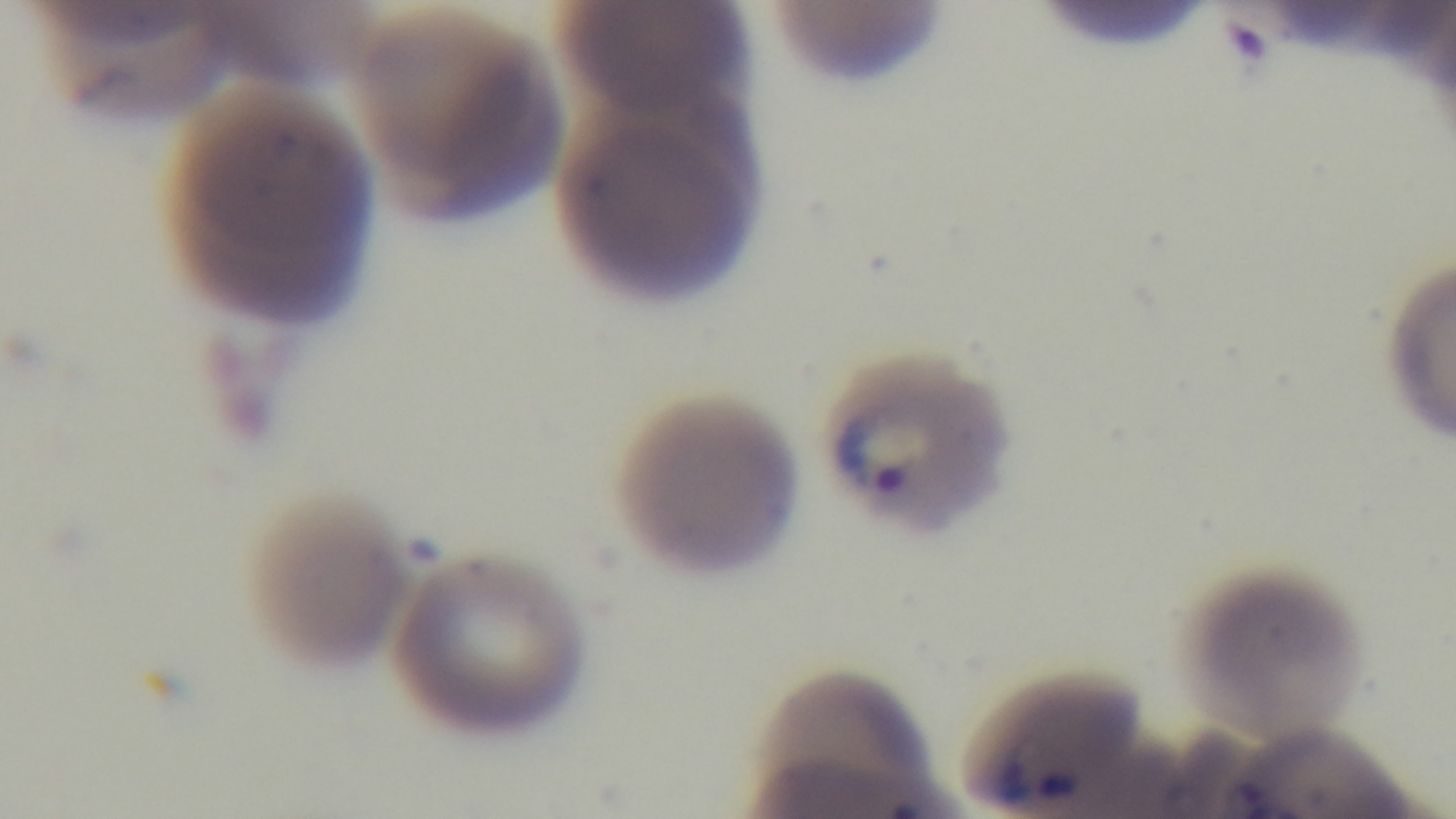

objective = 100x oil immersion
preparation = thin smear
field of view = single
stain = Giemsa
capture = mounted 4K digital camera
malaria status = infected
modality = light microscopy